Describe the morphology of the erythrocytes.
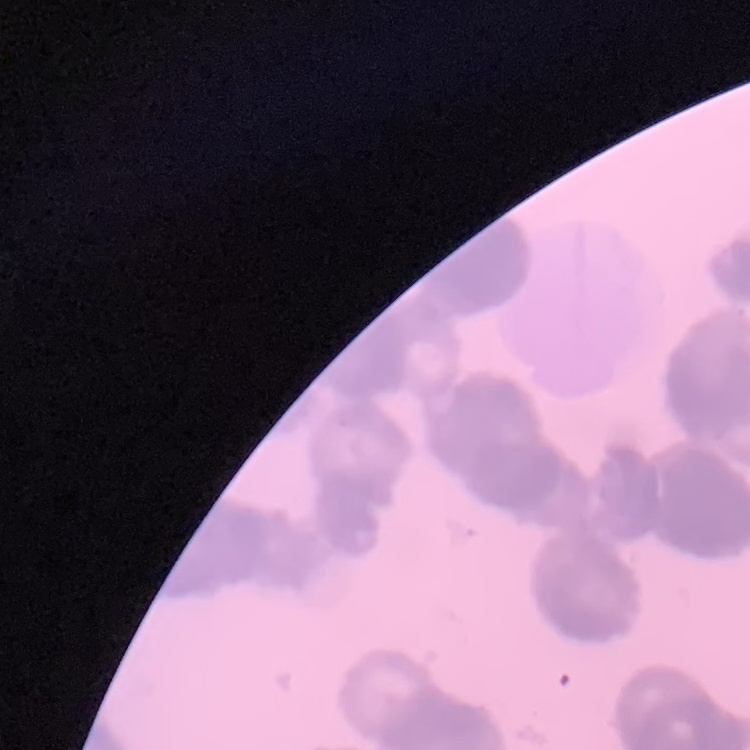

Rouleaux formation.

Stained with either Field's or Giemsa. One tile cut from a larger photomicrograph. Thin peripheral smear.